Describe the morphology of the red blood cells.
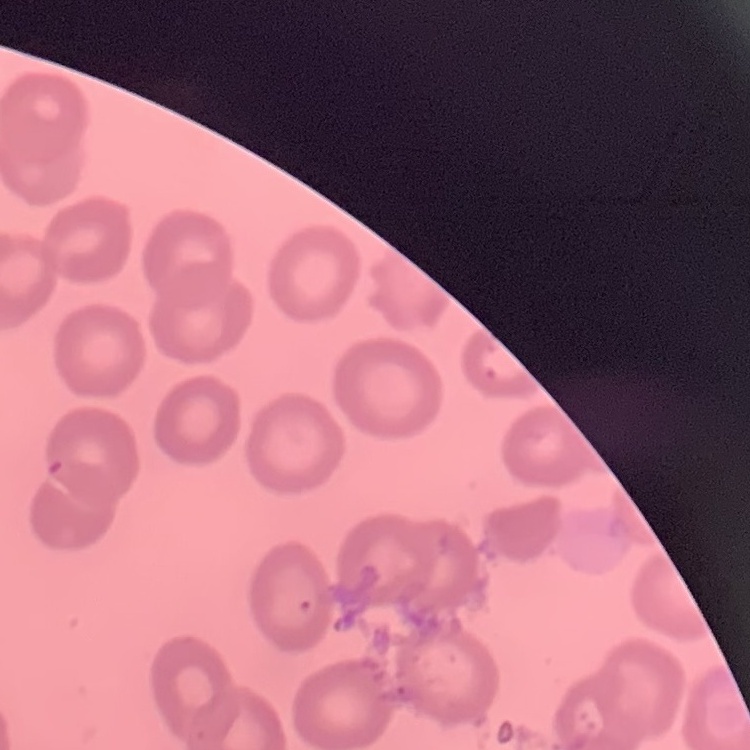

They show no rouleaux formation.

Summary:
  - Preparation: thin blood film
  - Stain: Field's or Giemsa
  - Image type: square crop of a larger photomicrograph